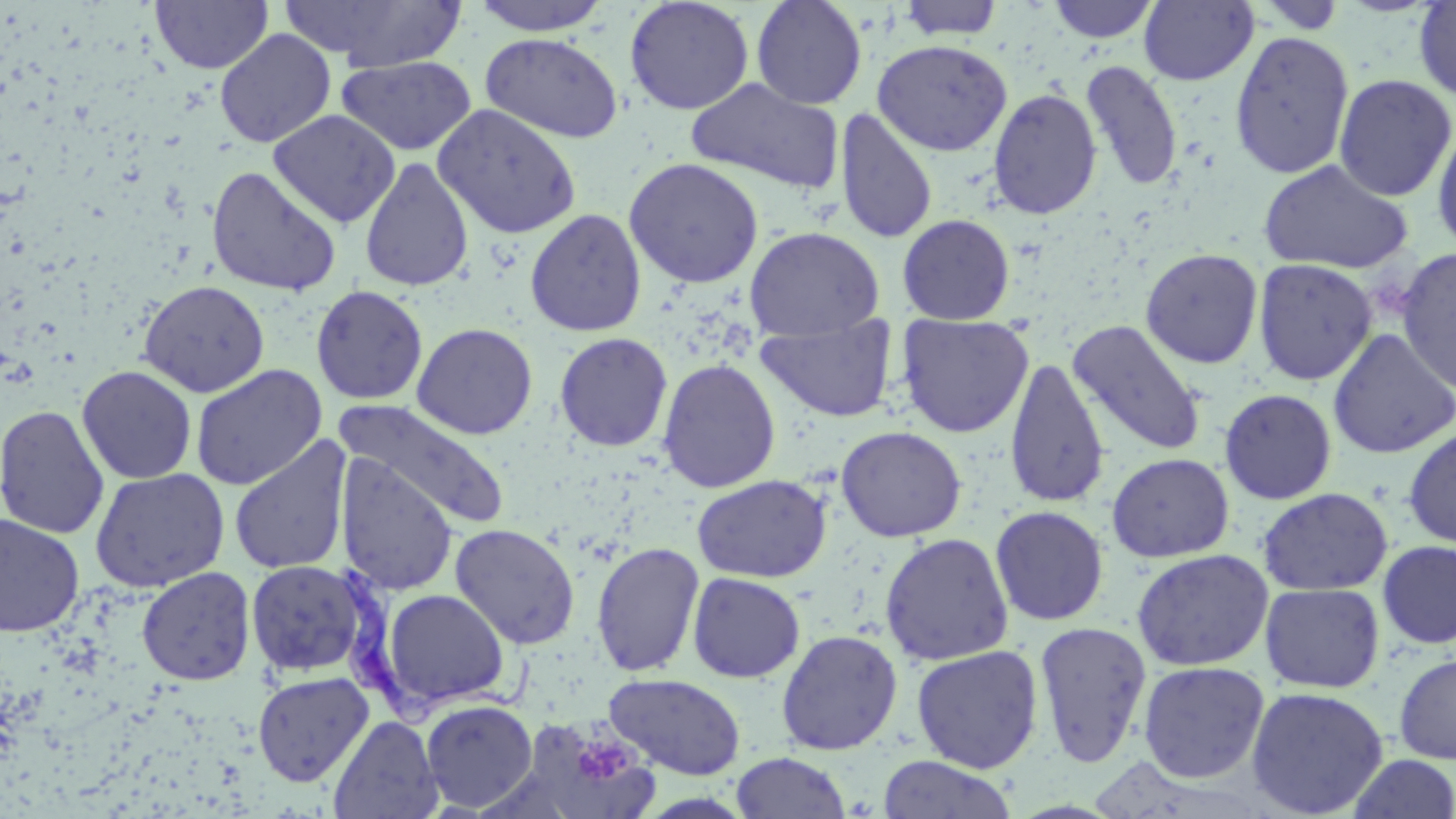
slide-level diagnosis = Trypanosoma brucei
magnification = 1000x
uninfected red blood cell locations = approximate bounding boxes as named x1/y1/x2/y2 corners in pixels: (x1=150, y1=0, x2=274, y2=73), (x1=280, y1=0, x2=468, y2=71), (x1=470, y1=0, x2=613, y2=35), (x1=751, y1=0, x2=867, y2=110), (x1=897, y1=0, x2=1005, y2=40), (x1=1046, y1=0, x2=1161, y2=43), (x1=1139, y1=0, x2=1258, y2=86), (x1=624, y1=1, x2=754, y2=115), (x1=1414, y1=1, x2=1456, y2=103), (x1=1248, y1=2, x2=1353, y2=35), (x1=214, y1=28, x2=336, y2=148), (x1=1229, y1=31, x2=1354, y2=180), (x1=480, y1=32, x2=624, y2=144), (x1=872, y1=39, x2=1013, y2=156), (x1=336, y1=55, x2=476, y2=155), (x1=1080, y1=60, x2=1184, y2=191), (x1=1334, y1=73, x2=1455, y2=202), (x1=686, y1=78, x2=844, y2=195), (x1=987, y1=87, x2=1102, y2=220), (x1=433, y1=104, x2=581, y2=239), (x1=835, y1=108, x2=937, y2=244), (x1=268, y1=109, x2=400, y2=228), (x1=1432, y1=121, x2=1456, y2=256), (x1=359, y1=157, x2=474, y2=292), (x1=623, y1=157, x2=764, y2=288), (x1=1257, y1=158, x2=1414, y2=274), (x1=206, y1=166, x2=342, y2=296), (x1=524, y1=208, x2=647, y2=337), (x1=897, y1=214, x2=1015, y2=325), (x1=744, y1=226, x2=884, y2=341), (x1=1395, y1=247, x2=1456, y2=396), (x1=1140, y1=248, x2=1263, y2=369), (x1=1253, y1=259, x2=1377, y2=386), (x1=139, y1=280, x2=269, y2=397), (x1=311, y1=285, x2=428, y2=405), (x1=897, y1=314, x2=1034, y2=438), (x1=757, y1=316, x2=897, y2=424), (x1=1067, y1=320, x2=1207, y2=456), (x1=412, y1=322, x2=538, y2=440), (x1=1328, y1=327, x2=1455, y2=459), (x1=554, y1=332, x2=673, y2=452), (x1=1004, y1=355, x2=1109, y2=509), (x1=658, y1=358, x2=780, y2=493), (x1=190, y1=364, x2=327, y2=490), (x1=77, y1=365, x2=197, y2=484), (x1=1219, y1=388, x2=1337, y2=504), (x1=335, y1=399, x2=511, y2=529), (x1=0, y1=403, x2=109, y2=540), (x1=836, y1=425, x2=966, y2=542), (x1=1402, y1=426, x2=1456, y2=549), (x1=228, y1=436, x2=353, y2=577), (x1=1106, y1=452, x2=1234, y2=562), (x1=336, y1=454, x2=458, y2=596), (x1=90, y1=468, x2=230, y2=593), (x1=691, y1=474, x2=831, y2=583), (x1=1257, y1=487, x2=1393, y2=596), (x1=991, y1=506, x2=1108, y2=626), (x1=0, y1=514, x2=85, y2=637), (x1=450, y1=523, x2=580, y2=649), (x1=879, y1=532, x2=1014, y2=665), (x1=1377, y1=540, x2=1456, y2=649), (x1=590, y1=541, x2=705, y2=677), (x1=1131, y1=549, x2=1274, y2=671), (x1=245, y1=559, x2=372, y2=678), (x1=136, y1=566, x2=256, y2=686), (x1=687, y1=572, x2=805, y2=683), (x1=1260, y1=582, x2=1386, y2=693), (x1=381, y1=589, x2=510, y2=711), (x1=1034, y1=621, x2=1152, y2=768), (x1=776, y1=629, x2=903, y2=755), (x1=911, y1=644, x2=1044, y2=774), (x1=1394, y1=653, x2=1456, y2=764), (x1=1138, y1=660, x2=1270, y2=783), (x1=252, y1=671, x2=374, y2=787), (x1=605, y1=673, x2=746, y2=779), (x1=1246, y1=686, x2=1388, y2=818), (x1=420, y1=699, x2=538, y2=812), (x1=329, y1=715, x2=443, y2=819), (x1=529, y1=720, x2=660, y2=819), (x1=730, y1=751, x2=851, y2=819), (x1=877, y1=754, x2=1017, y2=819), (x1=1346, y1=754, x2=1456, y2=818)
preparation = thin blood smear
stain = May-Grünwald-Giemsa
Trypanosoma brucei locations = approximate bounding boxes as named x1/y1/x2/y2 corners in pixels: (x1=330, y1=562, x2=542, y2=723)
field of view = one of a larger specimen
modality = optical microscopy
platelet locations = approximate bounding boxes as named x1/y1/x2/y2 corners in pixels: (x1=581, y1=741, x2=629, y2=780)
image size = 1456×819 pixels